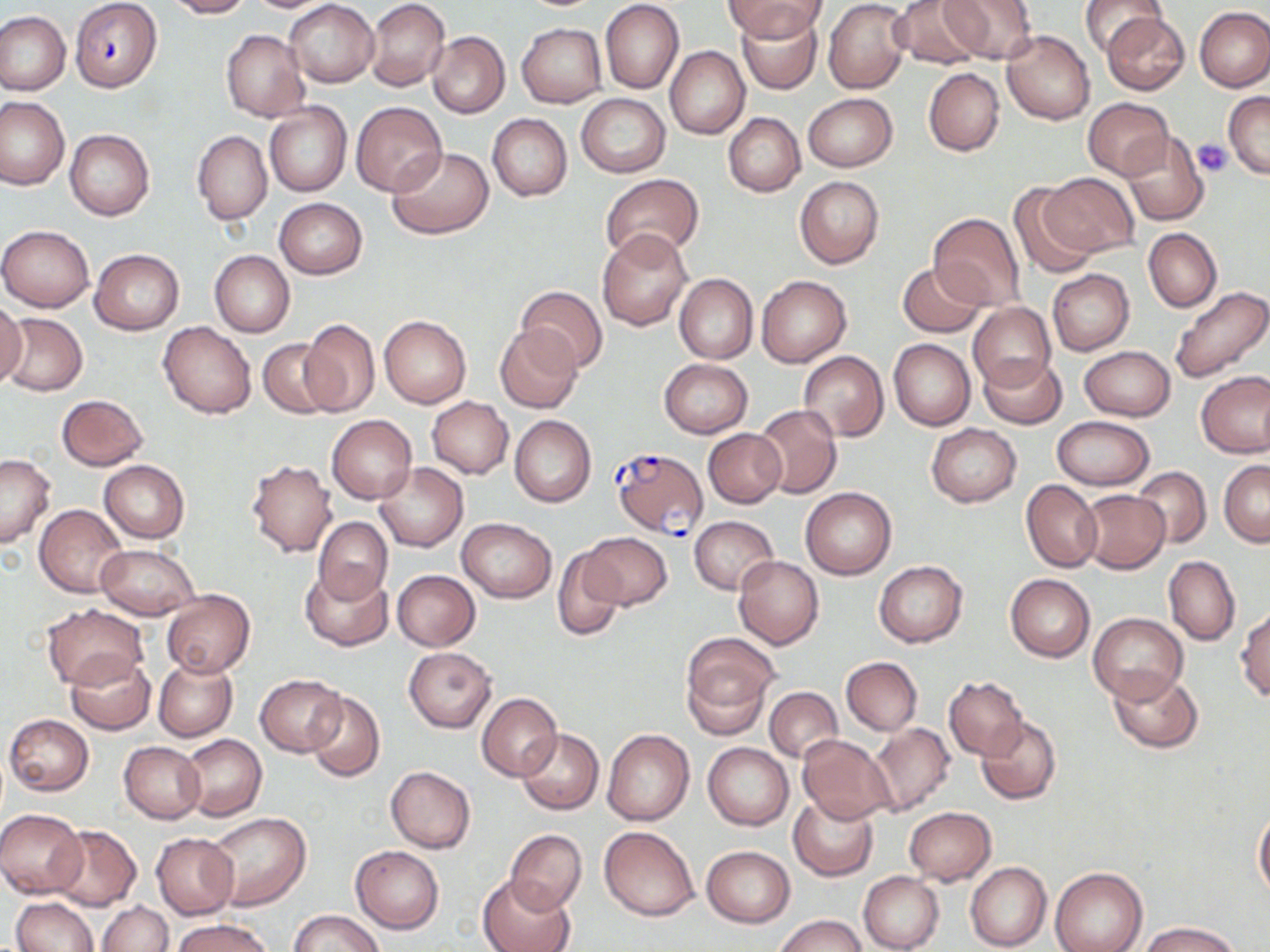
Summary:
  - Coordinate format: approximate bounding boxes as [x1, y1, x2, y2] in pixels
  - Plasmodium falciparum-infected red blood cell locations: [70, 0, 163, 92], [609, 447, 708, 538]
  - Platelet locations: [1194, 140, 1231, 177]
  - Uninfected red blood cell locations: [164, 0, 253, 18], [239, 0, 343, 13], [284, 0, 379, 87], [365, 0, 450, 91], [728, 0, 824, 42], [823, 0, 910, 94], [891, 0, 986, 69], [938, 0, 1038, 64], [1080, 0, 1165, 59], [600, 1, 684, 94], [1195, 7, 1270, 92], [738, 8, 822, 95], [0, 11, 70, 94], [1100, 12, 1188, 94], [516, 22, 607, 106], [221, 29, 308, 122], [1001, 30, 1095, 125], [427, 31, 510, 118], [665, 46, 749, 139], [924, 68, 1004, 156], [1224, 91, 1270, 179], [803, 93, 898, 171], [577, 94, 669, 178], [0, 95, 69, 190], [1084, 98, 1175, 180], [263, 101, 352, 197], [351, 102, 447, 196], [723, 112, 804, 196], [488, 114, 572, 201], [65, 129, 154, 220], [1121, 129, 1209, 226], [192, 130, 272, 225], [387, 146, 494, 239], [1038, 172, 1138, 258], [600, 174, 704, 263], [794, 176, 884, 268], [1009, 182, 1098, 281], [275, 198, 367, 279], [929, 211, 1026, 310], [0, 224, 94, 312], [1144, 228, 1222, 313], [597, 229, 691, 331], [90, 249, 184, 333], [209, 250, 294, 337], [897, 262, 987, 337], [1048, 270, 1133, 354], [673, 273, 758, 362], [756, 274, 851, 367], [1170, 285, 1270, 384], [517, 286, 608, 374], [0, 298, 26, 388], [968, 303, 1056, 390], [1, 312, 87, 396], [379, 314, 471, 408], [300, 320, 380, 418], [158, 322, 256, 418], [495, 325, 582, 412], [258, 338, 335, 418], [889, 338, 975, 431], [1079, 345, 1175, 420], [799, 351, 888, 441], [978, 353, 1067, 429], [658, 359, 753, 438], [1196, 372, 1270, 458], [56, 393, 148, 470], [427, 397, 514, 478], [753, 404, 842, 498], [510, 415, 596, 507], [326, 416, 416, 504], [1052, 417, 1154, 490], [927, 424, 1021, 506], [703, 429, 787, 509], [0, 454, 56, 549], [247, 459, 337, 556], [100, 460, 190, 542], [1219, 460, 1270, 546], [374, 463, 468, 552], [1133, 467, 1212, 549], [1021, 479, 1102, 572], [800, 487, 896, 580], [1076, 489, 1170, 574], [34, 505, 127, 598], [689, 515, 778, 595], [312, 516, 392, 602], [457, 518, 556, 602], [581, 532, 671, 609], [95, 545, 200, 619], [551, 547, 629, 642], [733, 556, 823, 649], [1163, 557, 1240, 645], [873, 560, 968, 647], [301, 566, 392, 650], [392, 569, 481, 650], [1006, 573, 1095, 661], [161, 591, 255, 677], [42, 604, 147, 690], [1235, 608, 1270, 701], [1088, 612, 1188, 704], [681, 634, 777, 736], [404, 647, 497, 733], [66, 653, 154, 735], [841, 656, 922, 735], [154, 657, 237, 742], [1107, 667, 1204, 754], [255, 674, 345, 755], [944, 676, 1028, 760], [765, 688, 842, 763], [305, 690, 386, 781], [479, 693, 561, 780], [4, 714, 94, 795], [975, 716, 1062, 804], [869, 722, 955, 816], [516, 728, 603, 816], [602, 729, 694, 825], [178, 734, 267, 820], [798, 734, 897, 823], [120, 741, 205, 823], [704, 743, 793, 830], [386, 766, 475, 853], [788, 795, 878, 880], [903, 807, 996, 885], [1254, 807, 1270, 901], [0, 810, 87, 898], [208, 812, 311, 910], [49, 825, 140, 911], [599, 826, 700, 922], [505, 829, 586, 914], [152, 834, 239, 919], [701, 845, 795, 927], [350, 846, 444, 932], [965, 862, 1052, 951], [1050, 868, 1147, 952], [859, 872, 944, 952], [478, 874, 575, 952], [12, 897, 99, 952], [99, 900, 171, 951], [289, 910, 383, 952], [778, 916, 867, 952], [172, 918, 273, 952], [1142, 921, 1240, 952]
  - Slide-level diagnosis: Plasmodium falciparum
  - Preparation: thin blood smear
  - Magnification: 1000x
  - Modality: optical microscopy
  - Field of view: single
  - Stain: May-Grünwald-Giemsa
  - Image size: 1270×952 pixels